Name the parasite shown.
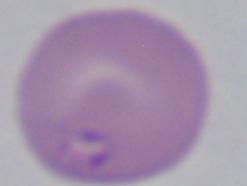
This is Babesia.

magnification = 1000x
modality = micrograph